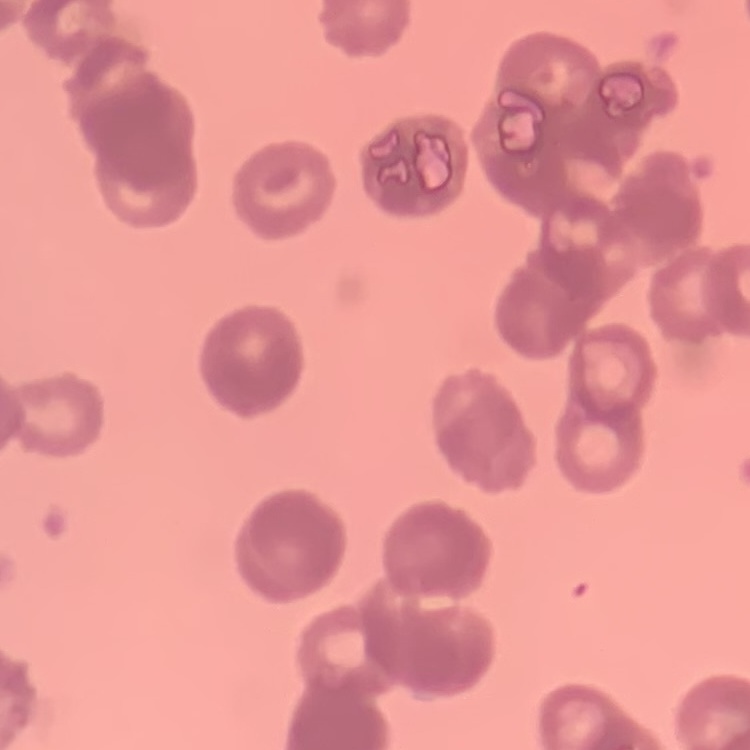
erythrocyte_morphology: rouleaux formation
image_type: square crop of a larger photomicrograph
stain: Field's or Giemsa
preparation: thin peripheral smear